Report the malaria status of this cell.
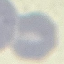

It is uninfected.

Summary:
  - Image type: automatically extracted cell patch, resized to 64 × 64 pixels
  - Preparation: thin smear
  - Stain: Giemsa
  - Capture: smartphone camera at the microscope eyepiece